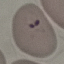
malaria status = parasitized
preparation = thin blood smear
image type = cell patch, automatically extracted from a larger field of view and resized to 64 × 64 pixels
capture = smartphone through the microscope eyepiece
stain = Giemsa